Assess this cell for malaria.
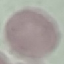
It is uninfected.

Summary:
  - Capture: smartphone camera at the microscope eyepiece
  - Preparation: thin blood smear
  - Image type: cell patch, automatically extracted from a larger field of view and resized to 64 × 64 pixels
  - Stain: Giemsa